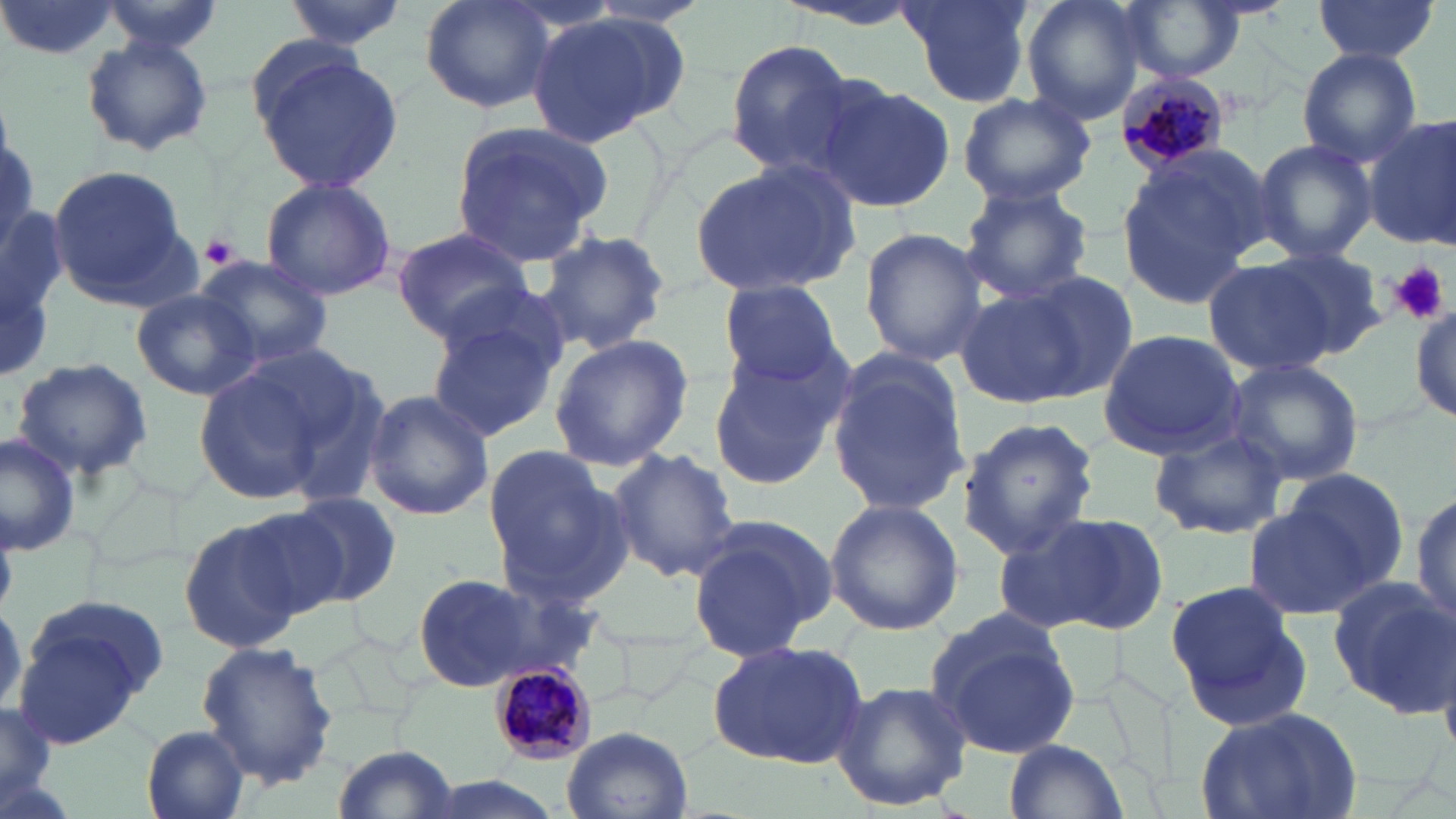

Plasmodium malariae-infected red blood cell locations = approximate bounding boxes as [x1, y1, x2, y2] in pixels: [1116, 70, 1231, 174], [488, 661, 601, 764]
slide-level diagnosis = Plasmodium malariae
magnification = 1000x
modality = optical microscopy
field of view = one of a larger specimen
preparation = thin blood film
stain = May-Grünwald-Giemsa
uninfected red blood cell locations = approximate bounding boxes as [x1, y1, x2, y2] in pixels: [0, 0, 122, 61], [280, 0, 408, 50], [417, 0, 559, 114], [770, 0, 930, 30], [895, 0, 1036, 108], [1020, 0, 1149, 124], [1116, 0, 1249, 84], [1312, 0, 1439, 62], [99, 1, 225, 57], [525, 11, 686, 145], [80, 34, 213, 156], [723, 40, 855, 174], [1296, 47, 1423, 168], [251, 48, 405, 195], [811, 79, 956, 213], [955, 91, 1094, 207], [1363, 115, 1456, 249], [448, 120, 611, 265], [1250, 139, 1378, 263], [1115, 149, 1265, 311], [691, 157, 860, 296], [46, 164, 193, 305], [259, 176, 398, 301], [957, 184, 1095, 306], [391, 226, 537, 341], [858, 228, 991, 366], [536, 229, 673, 356], [1264, 249, 1387, 357], [193, 254, 335, 370], [1202, 259, 1333, 377], [1010, 270, 1140, 399], [717, 279, 844, 386], [954, 287, 1092, 406], [129, 289, 264, 402], [1409, 304, 1456, 424], [425, 313, 562, 445], [1096, 329, 1246, 460], [547, 334, 695, 471], [705, 343, 850, 490], [826, 354, 971, 517], [10, 357, 153, 481], [1226, 358, 1364, 487], [194, 363, 337, 506], [361, 388, 495, 521], [956, 418, 1099, 559], [1148, 428, 1288, 540], [0, 433, 81, 555], [480, 442, 634, 610], [605, 447, 740, 580], [1262, 471, 1414, 615], [1410, 489, 1456, 634], [288, 492, 403, 605], [824, 498, 964, 636], [233, 502, 365, 620], [1001, 510, 1169, 638], [176, 514, 313, 654], [687, 516, 836, 662], [406, 571, 579, 692], [1325, 576, 1454, 716], [1164, 580, 1314, 732], [12, 599, 164, 748], [926, 612, 1083, 757], [707, 638, 870, 769], [196, 642, 338, 787], [831, 679, 973, 812], [0, 697, 57, 812], [1190, 703, 1365, 819], [140, 725, 253, 819], [559, 725, 692, 819], [1007, 738, 1126, 817], [331, 745, 462, 819]
image size = 1456×819 pixels
platelet locations = approximate bounding boxes as [x1, y1, x2, y2] in pixels: [200, 232, 242, 270], [1392, 261, 1450, 326]